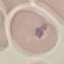
Malaria status: parasitized. Automatically extracted cell patch, resized to 64 × 64 pixels. Thin smear of blood. Photographed with a smartphone camera at the microscope eyepiece. Giemsa stain.